State the blood parasite species.
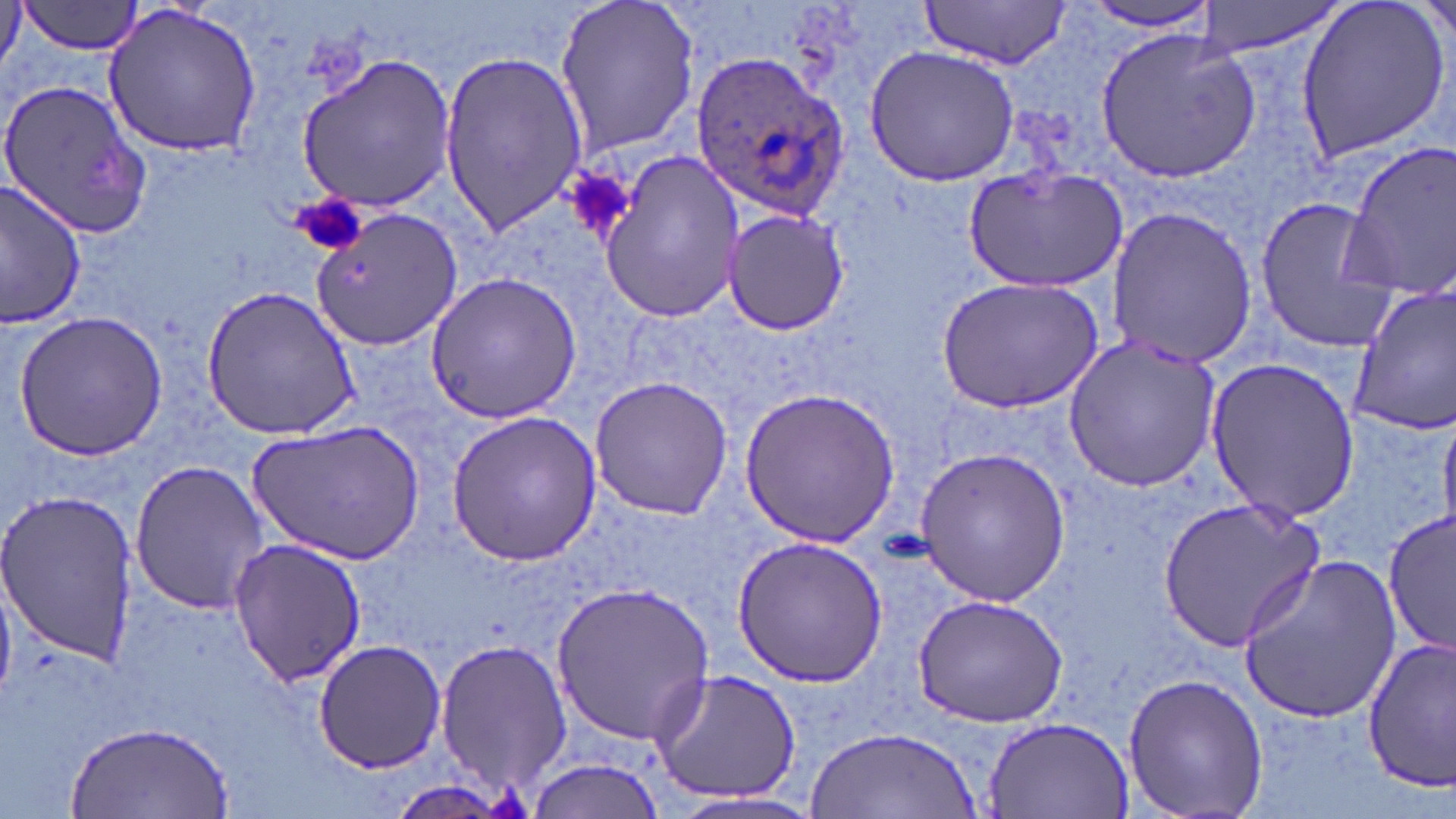
Plasmodium ovale.

Summary:
  - Coordinate format: approximate bounding boxes as (x1, y1, x2, y2) in pixels
  - Plasmodium ovale-infected red blood cell locations: (690, 48, 849, 218)
  - Platelet locations: (557, 164, 636, 246), (289, 192, 370, 258)
  - Uninfected red blood cell locations: (552, 0, 703, 158), (916, 0, 1074, 68), (1189, 0, 1351, 58), (1293, 0, 1448, 164), (1414, 0, 1454, 45), (19, 2, 148, 55), (1077, 3, 1224, 35), (101, 5, 264, 157), (1096, 28, 1261, 182), (863, 45, 1021, 185), (437, 48, 589, 237), (295, 55, 456, 209), (0, 76, 153, 238), (1337, 141, 1456, 299), (596, 150, 743, 325), (962, 165, 1129, 293), (1, 181, 87, 328), (1252, 193, 1396, 352), (1104, 205, 1258, 371), (312, 207, 464, 347), (721, 207, 852, 336), (425, 273, 583, 424), (935, 278, 1103, 415), (1348, 283, 1456, 436), (201, 286, 362, 439), (13, 312, 168, 461), (1062, 334, 1223, 492), (1205, 356, 1361, 521), (590, 375, 735, 519), (739, 387, 900, 548), (1440, 409, 1456, 532), (446, 410, 601, 564), (252, 418, 425, 564), (914, 445, 1071, 606), (129, 459, 268, 615), (0, 487, 139, 670), (1154, 495, 1325, 653), (1383, 508, 1454, 657), (733, 536, 889, 685), (228, 537, 368, 687), (1237, 555, 1402, 723), (551, 580, 713, 745), (913, 594, 1069, 726), (435, 637, 571, 793), (314, 640, 446, 771), (1362, 641, 1456, 789), (649, 665, 804, 805), (1120, 671, 1269, 819), (984, 714, 1135, 818), (67, 722, 233, 816), (808, 728, 979, 817), (526, 755, 667, 816), (669, 793, 828, 819)
  - Field of view: single
  - Stain: May-Grünwald-Giemsa
  - Preparation: thin blood film
  - Modality: light microscopy
  - Magnification: 1000x
  - Image size: 1456×819 pixels